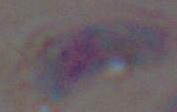

modality = photomicrograph
magnification = 1000x
identification = Toxoplasma gondii